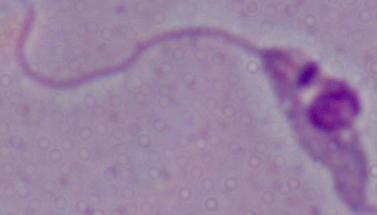
Captured at 1000x magnification. Micrograph. A Leishmania parasite is shown.